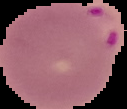
result: Plasmodium parasites identified
image_type: segmented cell region with the area outside set to black
preparation: thin blood smear
image_size: 127×109 pixels